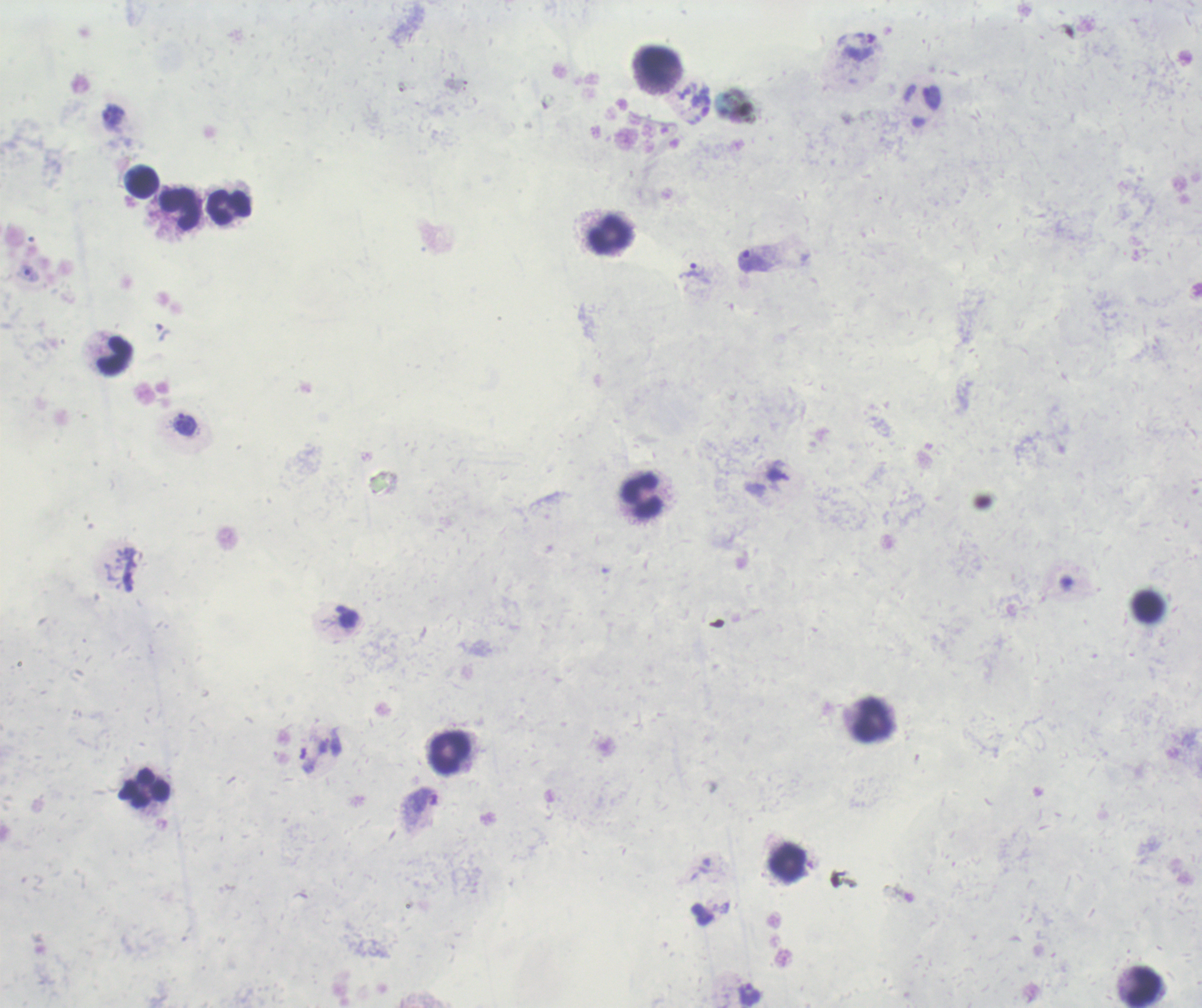

background_quality: poor
coloration_quality: bad
stain: Romanowsky
field_of_view: single
trophozoite_locations: 'approximate centers as {x, y} in pixels: {113, 115}, {754, 261}, {691, 270}, {184, 424}, {749, 994}'
leukocyte_locations: 'approximate centers as {x, y} in pixels: {659, 65}, {142, 183}, {227, 207}, {179, 209}, {609, 234}, {115, 356}, {641, 496}, {1147, 606}, {872, 719}, {449, 752}, {145, 788}, {788, 861}, {1142, 986}'
context: previously used in a real diagnosis
result: Plasmodium parasites identified
magnification: 100x
preparation: thick blood film
image_size: 1202×1008 pixels